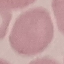
Summary:
  - Malaria status: uninfected
  - Preparation: thin smear
  - Stain: Giemsa
  - Capture: smartphone camera at the microscope eyepiece
  - Image type: automatically extracted cell patch, resized to 64 × 64 pixels